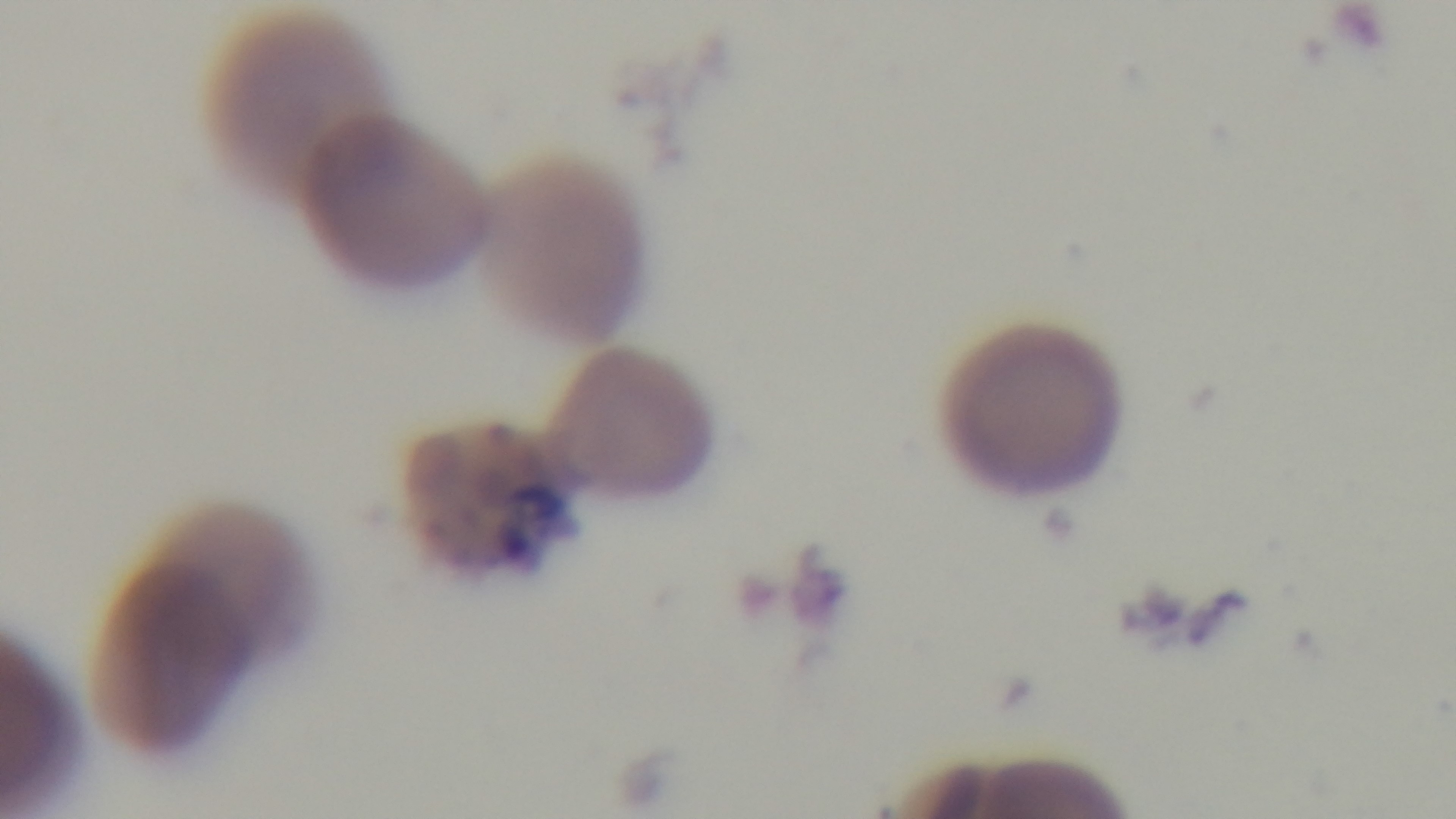
Mounted 4K digital camera. Preparation: thin smear. 100x oil-immersion objective. Giemsa stain. One field from the slide. Photomicrograph. Malaria status: infected.